Locate every leukocyte (white blood cell).
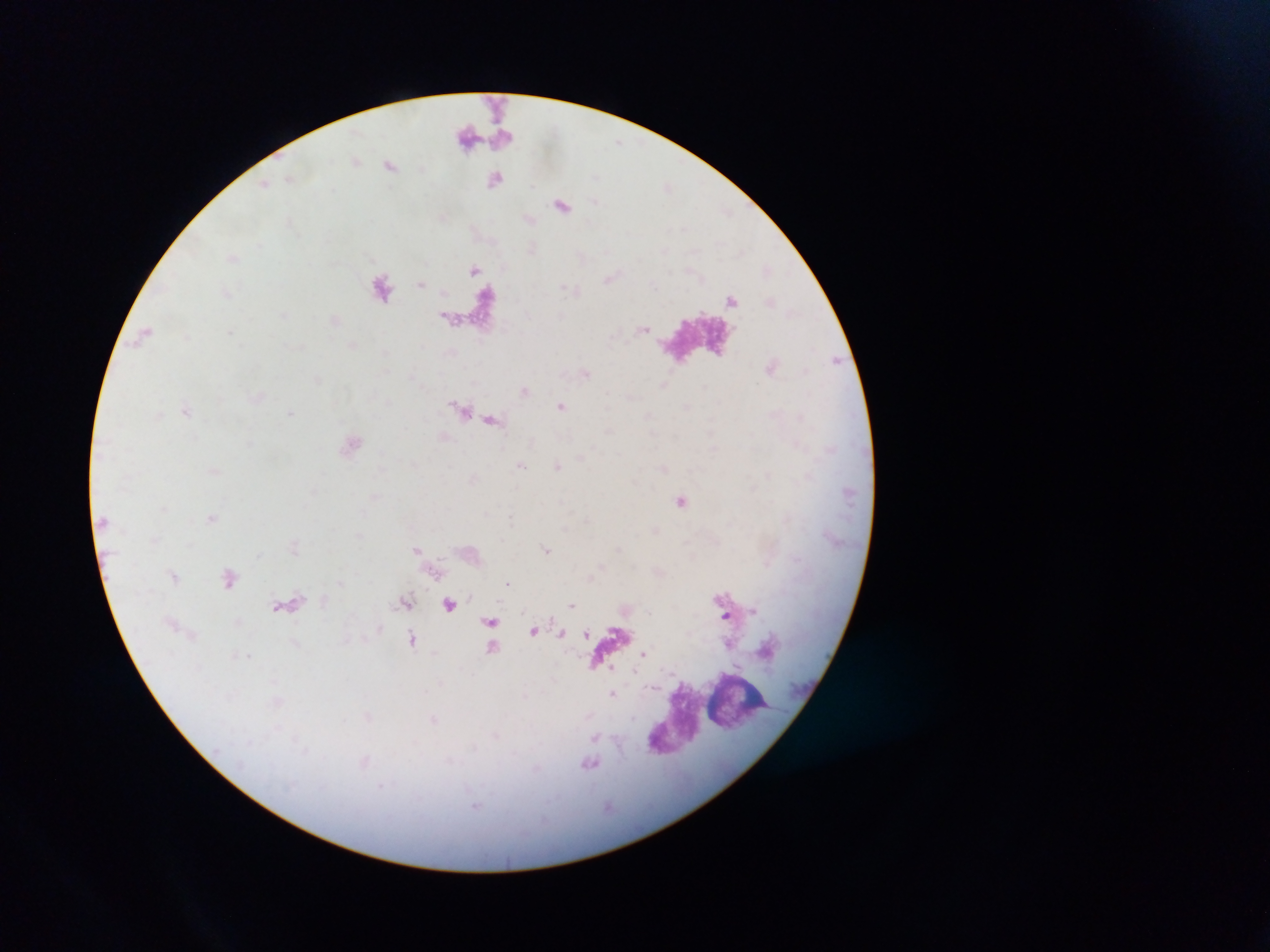
Approximate centers as (x, y) in pixels.
Leukocytes: (739, 697), (674, 719).

image_size: 1270×952 pixels
country: Ghana
capture: mobile-phone photograph through a microscope
plasmodium_parasite_locations: 'approximate centers as (x, y) in pixels: (288, 179), (232, 257), (230, 331), (560, 406), (186, 411), (291, 413), (521, 464), (558, 465), (681, 501), (211, 519), (417, 549), (546, 550), (507, 582), (572, 604), (753, 610), (726, 615), (533, 631), (586, 632), (561, 633), (412, 640), (643, 653), (250, 656), (612, 668), (636, 671), (611, 695), (434, 720), (589, 764)'
field_of_view: single
preparation: thick blood smear